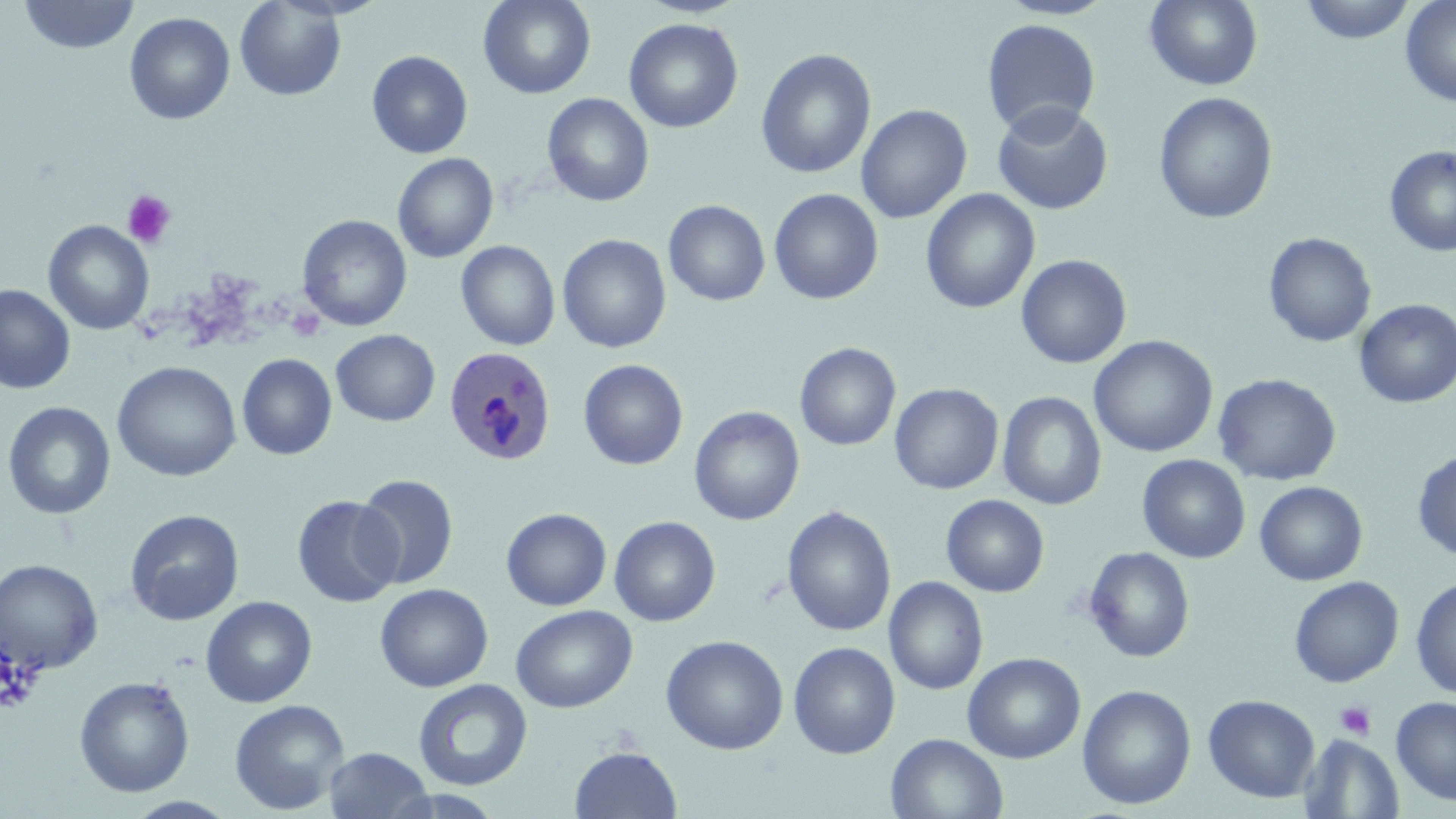

Approximate bounding boxes as [x1, y1, x2, y2] in pixels. Plasmodium ovale-infected red blood cell locations: [444, 346, 555, 466]. Platelet locations: [121, 190, 177, 248], [287, 309, 325, 342], [1, 649, 42, 714], [1335, 702, 1376, 739]. Uninfected red blood cell locations: [18, 0, 140, 55], [478, 0, 596, 99], [997, 0, 1118, 20], [1145, 0, 1263, 91], [1298, 0, 1417, 44], [1400, 0, 1456, 107], [234, 1, 347, 101], [124, 12, 235, 125], [624, 18, 743, 134], [981, 18, 1102, 136], [756, 49, 876, 178], [366, 50, 474, 159], [1154, 91, 1278, 225], [542, 93, 654, 207], [991, 101, 1114, 215], [856, 104, 973, 223], [1384, 145, 1456, 257], [392, 153, 498, 263], [769, 188, 884, 305], [920, 188, 1040, 314], [663, 200, 771, 306], [296, 214, 413, 331], [43, 220, 155, 336], [1263, 231, 1377, 348], [557, 234, 672, 353], [456, 240, 561, 351], [1015, 254, 1132, 369], [0, 284, 75, 394], [1354, 299, 1456, 409], [330, 329, 440, 426], [1089, 335, 1219, 458], [795, 342, 901, 451], [236, 354, 337, 460], [578, 359, 688, 470], [111, 361, 241, 482], [1213, 373, 1342, 487], [889, 383, 1004, 495], [997, 391, 1107, 511], [3, 401, 117, 520], [689, 406, 805, 525], [1412, 449, 1456, 561], [1136, 454, 1251, 563], [353, 473, 460, 590], [1254, 481, 1368, 586], [940, 494, 1049, 597], [291, 495, 404, 607], [782, 506, 897, 637], [501, 507, 612, 611], [125, 509, 245, 626], [609, 516, 721, 627], [1084, 546, 1195, 663], [0, 558, 104, 674], [884, 576, 988, 696], [1288, 576, 1404, 688], [1411, 577, 1456, 699], [374, 583, 493, 692], [201, 596, 318, 708], [510, 604, 637, 713], [661, 634, 789, 755], [788, 641, 900, 759], [962, 651, 1086, 764], [74, 675, 195, 797], [413, 678, 533, 791], [1077, 684, 1197, 810], [1203, 694, 1320, 803], [1391, 696, 1456, 805], [229, 699, 349, 814], [885, 732, 1009, 819], [1299, 734, 1404, 818], [570, 745, 682, 819], [324, 747, 435, 819]. Slide-level diagnosis: Plasmodium ovale. Captured at 1000x magnification. Single field of view. Optical microscopy. Thin blood smear. Image is 1456×819 pixels. May-Grünwald-Giemsa-stained preparation.